Locate and identify every blood parasite.
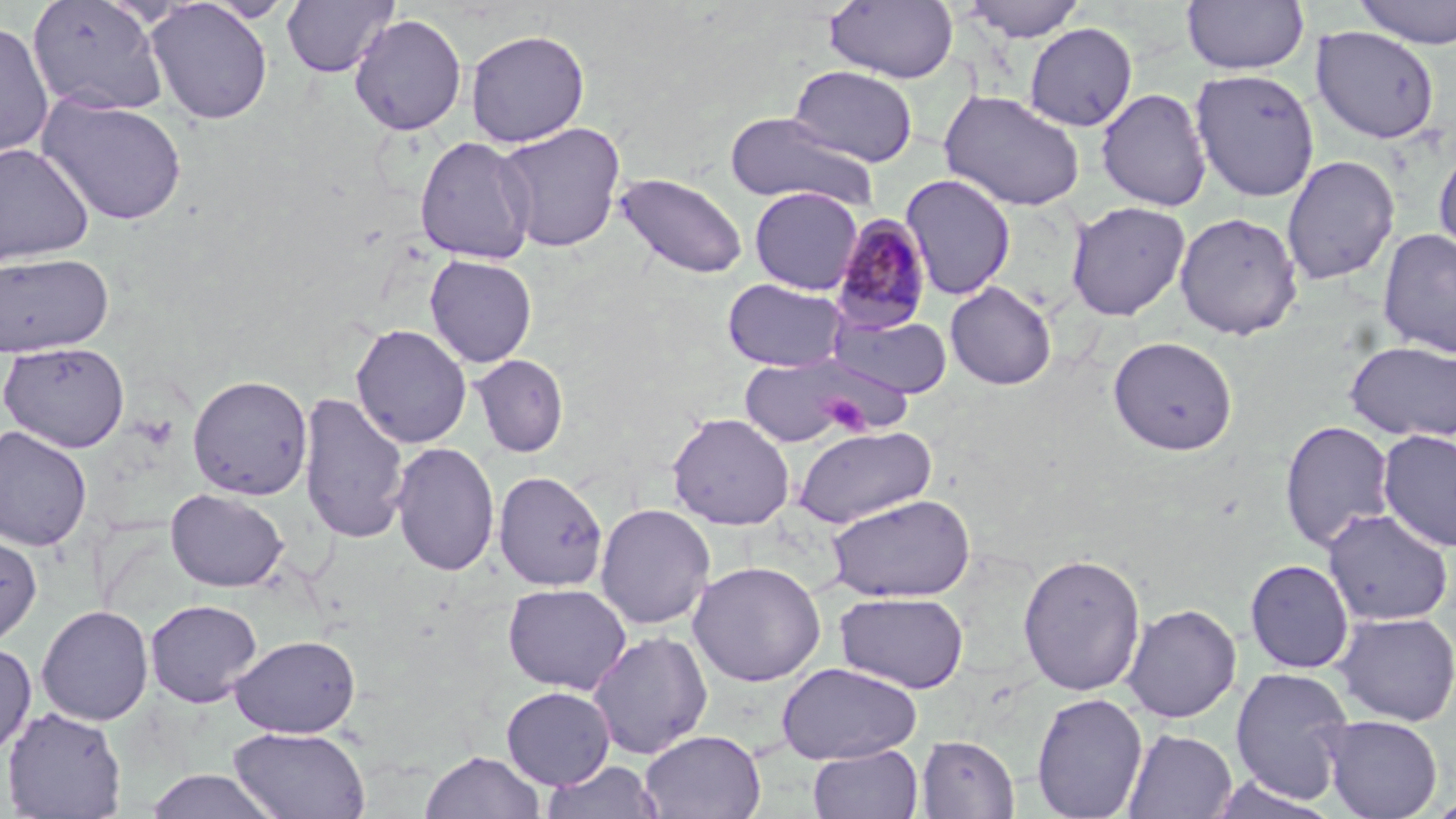
Approximate bounding boxes as [x1, y1, x2, y2] in pixels.
Plasmodium malariae-infected red blood cells: [829, 213, 934, 335].
No Plasmodium falciparum, Plasmodium ovale, Plasmodium vivax, Babesia divergens, or Trypanosoma brucei observed.

slide-level diagnosis = Plasmodium malariae
preparation = thin blood smear
magnification = 1000x
modality = light microscopy
field of view = one of a larger specimen
stain = May-Grünwald-Giemsa
platelet locations = approximate bounding boxes as [x1, y1, x2, y2] in pixels: [820, 393, 874, 436]
uninfected red blood cell locations = approximate bounding boxes as [x1, y1, x2, y2] in pixels: [27, 0, 170, 117], [281, 0, 399, 78], [824, 0, 959, 84], [960, 0, 1088, 42], [1181, 0, 1310, 75], [1354, 0, 1456, 49], [146, 1, 273, 125], [349, 14, 467, 136], [0, 20, 55, 159], [1024, 22, 1138, 131], [1311, 26, 1440, 144], [465, 29, 590, 147], [788, 65, 918, 167], [1189, 68, 1320, 202], [1096, 87, 1212, 211], [939, 89, 1086, 212], [37, 96, 188, 226], [724, 112, 878, 211], [494, 122, 626, 253], [414, 136, 537, 264], [0, 143, 95, 266], [1434, 145, 1456, 262], [1282, 155, 1399, 287], [615, 172, 749, 279], [900, 174, 1016, 300], [749, 187, 863, 294], [1066, 201, 1191, 321], [1175, 211, 1303, 340], [1377, 228, 1456, 359], [0, 252, 114, 357], [424, 255, 538, 368], [722, 277, 848, 372], [944, 281, 1057, 390], [831, 312, 953, 398], [351, 324, 473, 449], [1108, 335, 1238, 456], [1345, 340, 1455, 442], [2, 341, 131, 453], [470, 353, 569, 458], [737, 353, 882, 447], [187, 374, 313, 500], [297, 391, 410, 546], [666, 412, 795, 530], [1279, 420, 1395, 552], [0, 425, 93, 551], [793, 425, 938, 528], [1377, 429, 1456, 552], [390, 441, 500, 577], [492, 469, 609, 592], [165, 488, 289, 592], [826, 493, 976, 603], [594, 503, 716, 630], [1322, 508, 1454, 626], [0, 526, 43, 649], [1018, 553, 1146, 695], [1245, 559, 1354, 673], [688, 560, 826, 687], [502, 582, 631, 694], [835, 591, 969, 694], [145, 599, 263, 707], [1121, 603, 1241, 723], [36, 605, 154, 726], [1332, 611, 1456, 726], [588, 630, 713, 759], [229, 634, 361, 738], [0, 642, 37, 759], [776, 662, 922, 764], [1229, 666, 1355, 803], [501, 686, 616, 789], [1031, 692, 1148, 818], [2, 706, 127, 819], [1320, 715, 1443, 818], [229, 727, 371, 818], [1122, 728, 1237, 818], [640, 729, 766, 818], [916, 735, 1020, 818], [808, 743, 923, 819], [420, 750, 544, 819], [541, 759, 664, 819], [143, 769, 281, 819], [1208, 776, 1340, 818]
image size = 1456×819 pixels